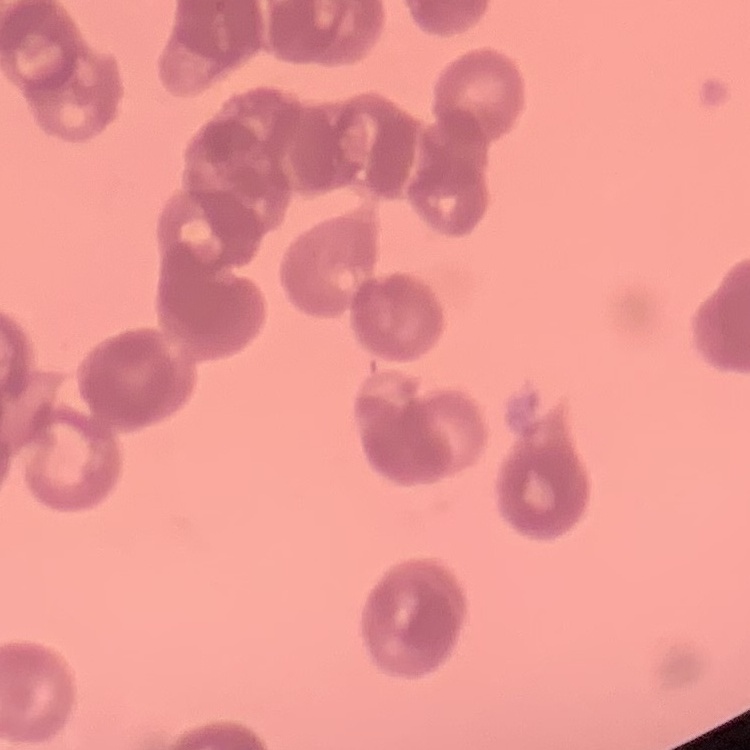 The erythrocytes exhibit rouleaux formation. Thin peripheral smear. Stained with either Field's or Giemsa. One tile cut from a larger photomicrograph.